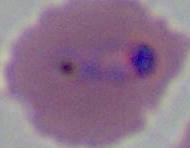
magnification: 400x or 1000x
modality: micrograph
identification: Plasmodium